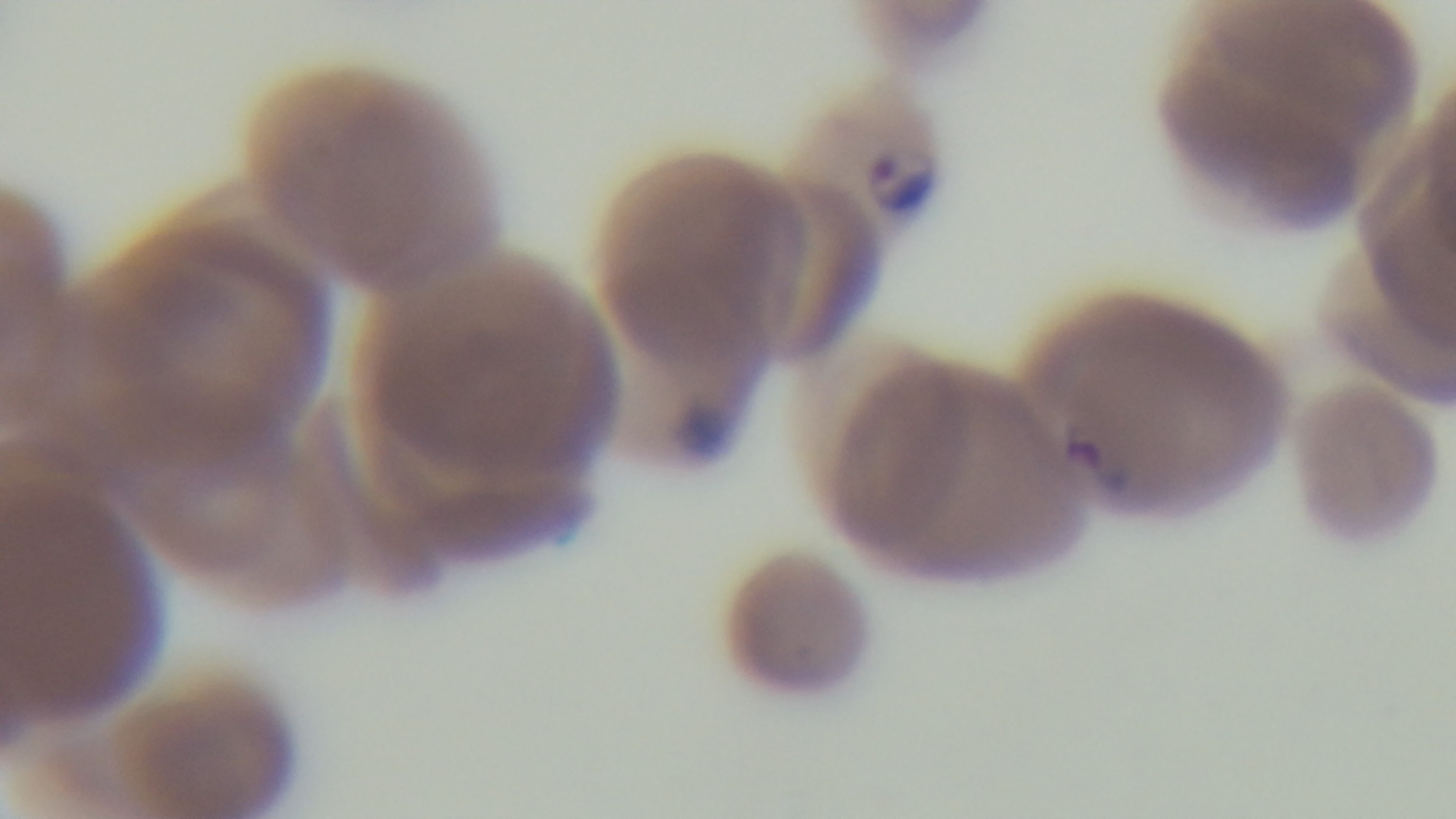

Preparation: thin smear. Single field of view. Malaria status: positive. Giemsa stain. Photomicrograph. 100x oil-immersion objective. Captured with a mounted 4K digital camera.